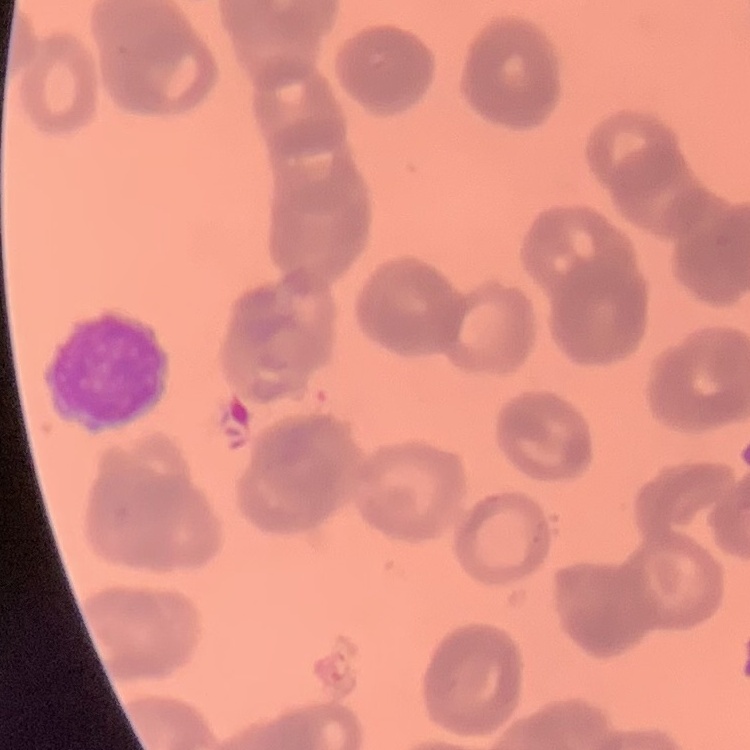
Summary:
  - Erythrocyte morphology: rouleaux formation
  - Image type: one tile cut from a larger photomicrograph
  - Stain: Field's or Giemsa
  - Preparation: thin blood film